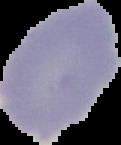
image type = cell region segmented out of the field of view; surrounding area masked to black
image size = 121×145 pixels
preparation = thin blood smear
result = no malaria parasites seen